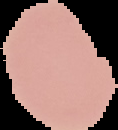
The area outside the segmented cell region is set to black. Malaria status: uninfected. Image is 118×130 pixels. From a thin blood film.